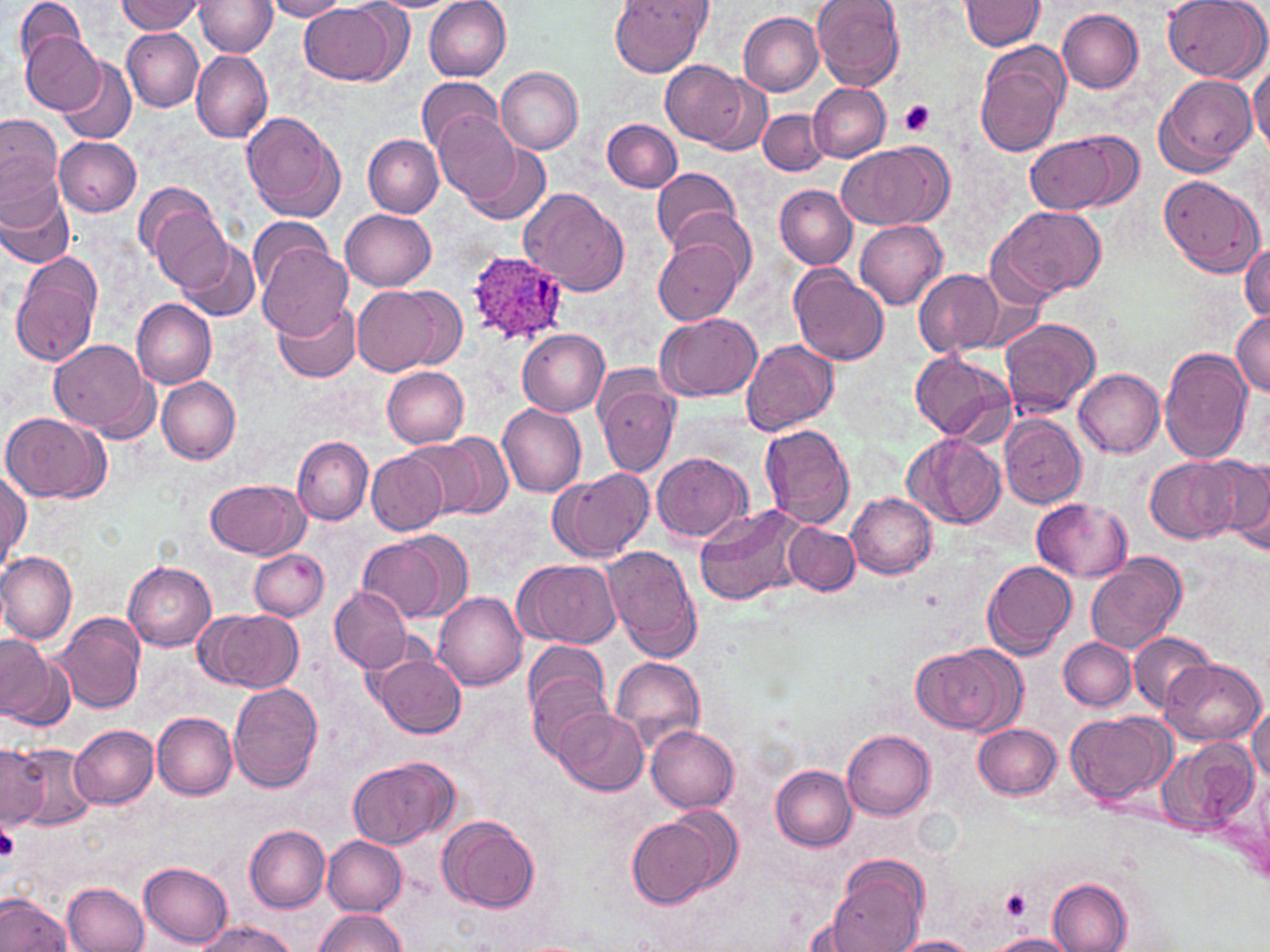

{
  "slide_level_diagnosis": "Plasmodium ovale",
  "preparation": "thin blood film",
  "plasmodium_ovale_infected_red_blood_cell_locations": "approximate bounding boxes as (x1,y1)-(x2,y2) corner pairs in pixels: (461,249)-(566,351)",
  "stain": "May-Grünwald-Giemsa",
  "modality": "light microscopy",
  "field_of_view": "single",
  "platelet_locations": "approximate bounding boxes as (x1,y1)-(x2,y2) corner pairs in pixels: (899,99)-(935,135), (0,822)-(21,863), (999,888)-(1033,923)",
  "uninfected_red_blood_cell_locations": "approximate bounding boxes as (x1,y1)-(x2,y2) corner pairs in pixels: (13,0)-(85,74), (264,0)-(350,21), (611,0)-(710,77), (812,0)-(905,90), (1161,0)-(1269,82), (117,1)-(207,35), (195,1)-(276,56), (366,1)-(467,13), (425,1)-(512,81), (962,1)-(1045,51), (299,2)-(405,85), (1057,8)-(1144,94), (739,12)-(823,96), (122,28)-(204,112), (20,32)-(105,114), (974,41)-(1071,159), (192,49)-(272,144), (54,58)-(136,145), (661,61)-(749,144), (1248,63)-(1270,153), (496,67)-(584,153), (703,74)-(773,157), (1154,74)-(1256,174), (416,75)-(502,158), (807,82)-(890,162), (239,109)-(346,222), (758,109)-(828,177), (434,114)-(522,206), (0,117)-(64,226), (603,119)-(682,192), (1024,131)-(1137,216), (55,137)-(142,217), (363,137)-(443,217), (458,138)-(552,227), (836,140)-(953,231), (652,166)-(740,256), (1158,175)-(1266,278), (775,185)-(857,269), (138,187)-(229,288), (519,188)-(630,296), (0,190)-(73,271), (993,206)-(1107,298), (341,208)-(435,291), (666,208)-(755,287), (249,216)-(336,295), (854,219)-(947,310), (173,237)-(261,322), (653,238)-(744,326), (258,241)-(353,340), (1239,242)-(1270,324), (11,252)-(103,366), (787,263)-(889,366), (913,268)-(1004,356), (350,284)-(456,376), (131,299)-(216,388), (270,300)-(360,383), (1232,312)-(1269,397), (656,314)-(761,402), (999,318)-(1100,417), (519,330)-(609,416), (741,339)-(838,436), (49,340)-(155,436), (1157,346)-(1252,464), (911,350)-(1013,443), (380,366)-(469,448), (1074,369)-(1165,456), (594,374)-(680,477), (156,377)-(241,464), (498,403)-(588,498), (2,412)-(108,502), (1001,416)-(1085,510), (760,423)-(855,532), (903,433)-(1006,531), (413,434)-(512,520), (293,436)-(372,524), (366,451)-(449,535), (652,452)-(750,544), (1207,455)-(1270,551), (1147,457)-(1240,543), (548,468)-(655,563), (0,469)-(30,570), (206,479)-(308,558), (846,493)-(938,580), (1033,499)-(1133,582), (694,504)-(813,609), (784,523)-(860,595), (358,537)-(451,623), (603,546)-(702,663), (250,548)-(327,620), (1,552)-(76,643), (1087,553)-(1187,654), (514,559)-(621,648), (981,560)-(1076,658), (124,561)-(216,651), (330,587)-(413,672), (434,592)-(528,690), (196,609)-(305,693), (54,612)-(146,714), (1126,632)-(1217,713), (0,635)-(65,729), (1060,637)-(1136,710), (911,643)-(1017,734), (371,652)-(467,738), (526,655)-(614,757), (611,656)-(706,751), (1162,659)-(1264,746), (229,681)-(322,792), (1247,705)-(1270,786), (554,709)-(648,796), (1066,710)-(1171,802), (152,712)-(238,799), (975,723)-(1060,800), (71,725)-(158,808), (647,725)-(740,812), (843,728)-(934,818), (1158,738)-(1258,835), (6,742)-(98,831), (1,744)-(49,828), (346,756)-(459,849), (771,764)-(858,849), (626,809)-(735,911), (438,814)-(540,914), (246,825)-(330,912), (323,836)-(406,913), (140,860)-(233,945), (825,870)-(923,952), (1049,878)-(1131,952), (61,881)-(149,952), (0,893)-(71,952), (312,908)-(407,951), (193,920)-(298,952), (988,933)-(1077,952), (893,937)-(979,952)",
  "magnification": "1000x",
  "image_size": "1270×952 pixels"
}